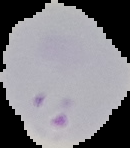 Result: malaria parasites identified. Cell region segmented out of the field of view; the surrounding area is masked to black. Image is 130×148 pixels. From a thin blood smear.